Assess this cell for malaria.
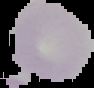

It is uninfected.

image size = 94×88 pixels
preparation = thin blood smear
image type = segmented cell region with the area outside set to black